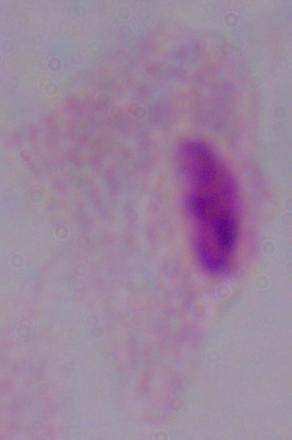
Summary:
  - Identification: trichomonad
  - Modality: photomicrograph
  - Magnification: 1000x